Assess this cell for malaria.
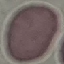

It is uninfected.

Photographed with a smartphone camera at the microscope eyepiece. Cell patch, automatically extracted from a larger field of view and resized to 64 × 64 pixels. Thin blood film. Giemsa stain.